Locate every blood parasite and identify its species.
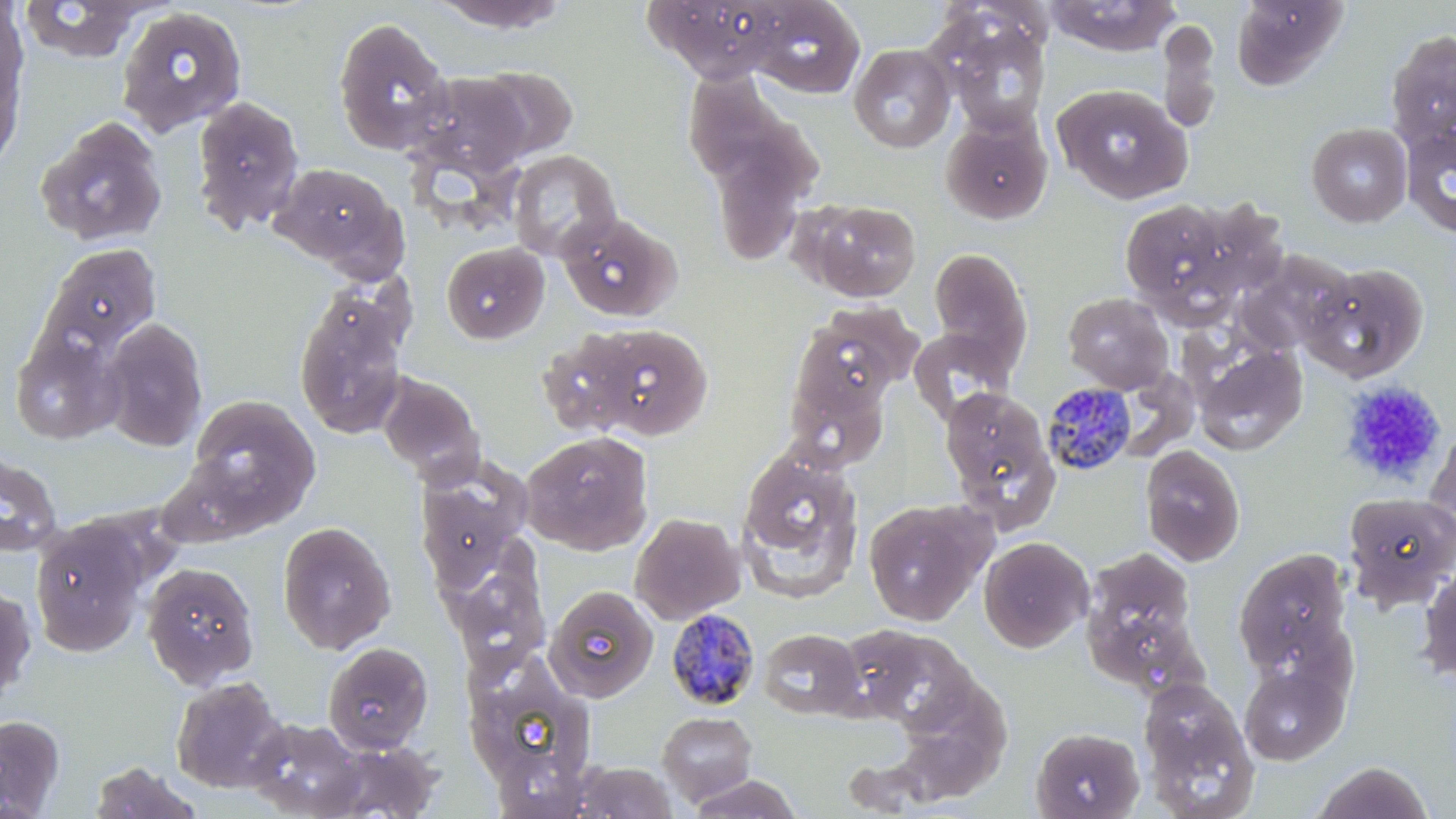

Approximate bounding boxes as [x1, y1, x2, y2] in pixels.
Plasmodium malariae-infected red blood cells: [1040, 382, 1139, 477], [664, 608, 761, 711].
No Plasmodium falciparum, Plasmodium ovale, Plasmodium vivax, Babesia divergens, or Trypanosoma brucei observed.

Platelet locations: [1339, 379, 1448, 487]. Uninfected red blood cell locations: [18, 0, 149, 64], [425, 0, 574, 33], [645, 0, 790, 83], [746, 0, 865, 98], [1045, 0, 1181, 56], [1230, 0, 1350, 90], [0, 1, 30, 106], [115, 5, 248, 138], [933, 11, 1052, 136], [332, 16, 453, 156], [1156, 18, 1222, 135], [1386, 30, 1456, 152], [0, 33, 26, 175], [849, 43, 956, 153], [672, 59, 791, 191], [468, 64, 580, 163], [408, 72, 535, 179], [1052, 83, 1193, 205], [190, 94, 306, 237], [940, 115, 1053, 224], [35, 117, 168, 248], [1306, 123, 1412, 228], [1402, 124, 1456, 238], [408, 131, 531, 237], [706, 133, 814, 269], [508, 149, 622, 261], [269, 162, 406, 275], [1117, 196, 1249, 317], [802, 198, 922, 302], [557, 211, 682, 322], [441, 241, 549, 345], [40, 243, 162, 356], [927, 247, 1033, 373], [1233, 252, 1356, 356], [1301, 262, 1430, 384], [292, 284, 411, 440], [1062, 291, 1174, 393], [810, 301, 923, 393], [100, 316, 208, 452], [780, 316, 907, 461], [581, 320, 715, 441], [908, 328, 1015, 424], [536, 330, 647, 439], [10, 331, 123, 445], [1190, 340, 1308, 455], [376, 372, 486, 484], [939, 387, 1061, 529], [187, 395, 320, 521], [1423, 421, 1456, 547], [520, 430, 654, 555], [1139, 444, 1246, 566], [734, 445, 865, 602], [0, 453, 62, 556], [415, 458, 533, 593], [1342, 492, 1456, 610], [862, 496, 993, 626], [630, 512, 745, 624], [30, 520, 148, 657], [277, 521, 396, 654], [978, 536, 1094, 653], [1081, 545, 1201, 684], [445, 547, 551, 675], [1232, 548, 1354, 679], [1417, 561, 1456, 688], [142, 562, 260, 687], [0, 584, 36, 707], [545, 586, 659, 702], [759, 628, 864, 719], [851, 628, 978, 733], [322, 641, 434, 754], [1239, 660, 1350, 765], [468, 669, 601, 790], [898, 675, 1016, 797], [170, 676, 288, 793], [1137, 677, 1260, 819], [657, 711, 758, 807], [0, 714, 66, 816], [246, 717, 369, 817], [1031, 726, 1145, 819], [322, 740, 444, 818], [1310, 760, 1436, 819], [87, 761, 203, 819], [570, 761, 678, 819], [687, 774, 803, 818]. Slide-level diagnosis: Plasmodium malariae. Thin blood film. One field of a larger specimen. Image is 1456×819 pixels. May-Grünwald-Giemsa stain. Light microscopy. 1000x magnification.